Assess the morphology of the erythrocytes.
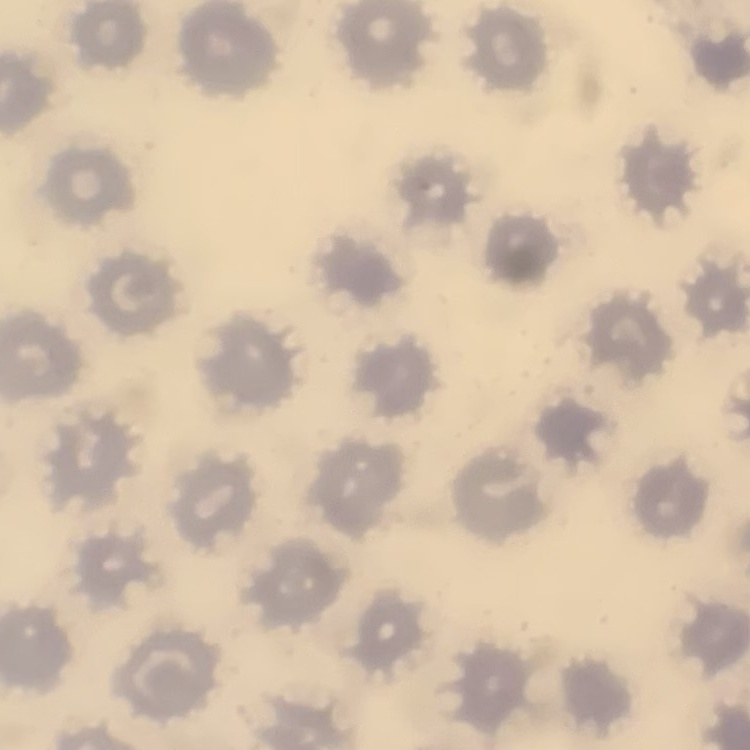

No rouleaux formation.

One tile cut from a larger photomicrograph. Field's or Giemsa stain. Thin blood film.